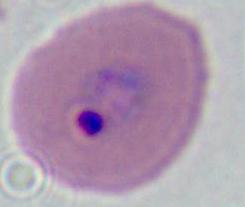 Micrograph. A Plasmodium parasite is shown. Captured at either 400x or 1000x magnification.